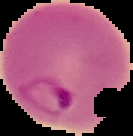
image_size: 133×136 pixels
malaria_status: parasitized
preparation: thin blood smear
image_type: cell region segmented out of the field of view; surrounding area masked to black